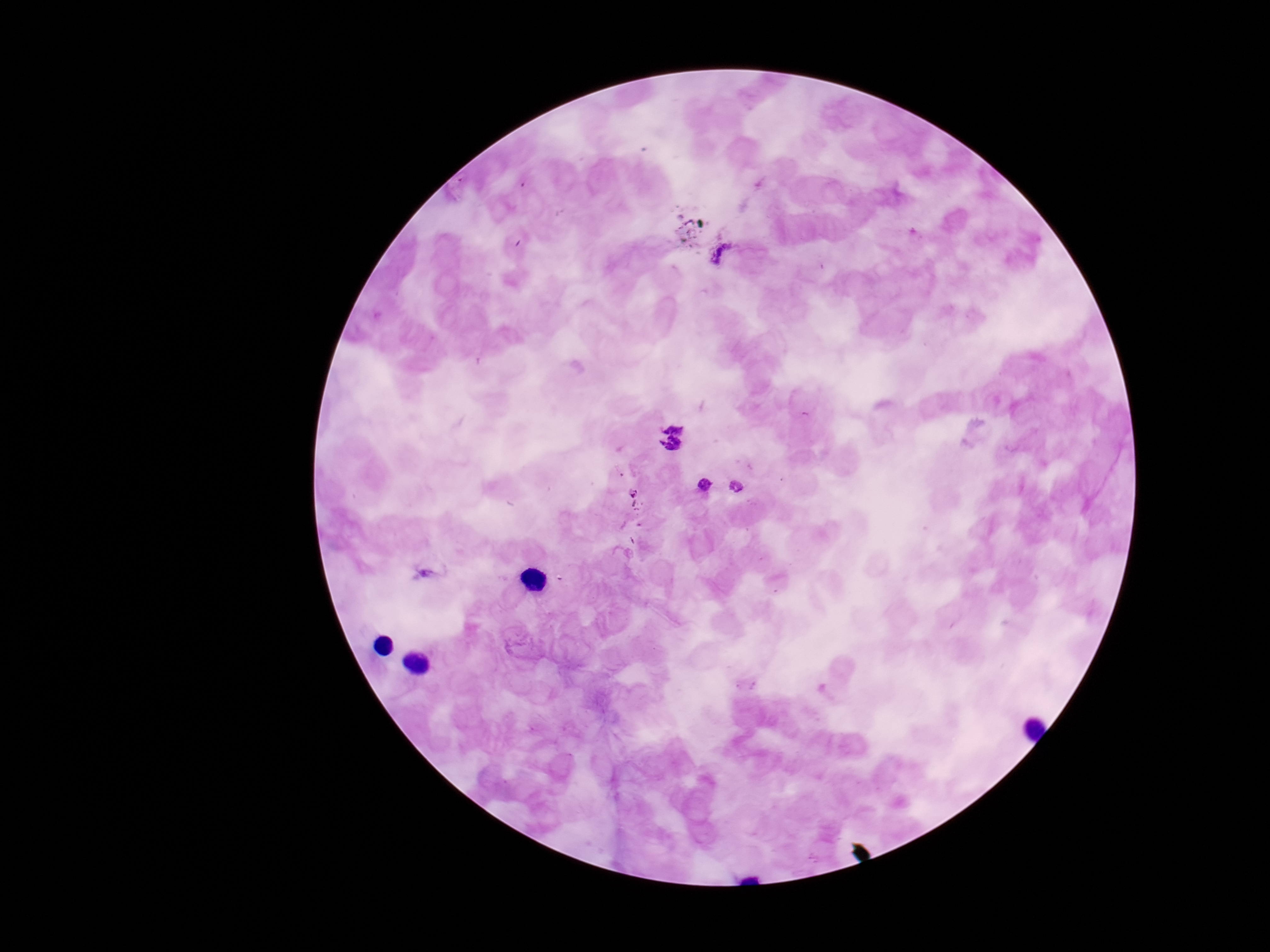

Approximate centers as {x, y} in pixels.
Summary:
  - Plasmodium parasite locations: {723, 252}, {674, 425}, {670, 447}, {705, 484}, {736, 485}
  - Magnification: 100x
  - Field of view: single
  - Capture: smartphone camera through the microscope eyepiece
  - Patient malaria status: positive
  - Stain: Giemsa
  - Image size: 1270×952 pixels
  - Preparation: thick blood smear